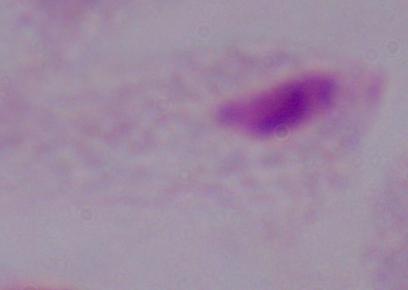

{
  "magnification": "1000x",
  "modality": "micrograph",
  "identification": "trichomonad"
}